Classify this cell by malaria status.
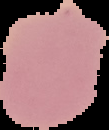

It is uninfected.

Summary:
  - Image size: 109×130 pixels
  - Image type: cell region segmented out of the field of view; surrounding area masked to black
  - Preparation: thin blood smear